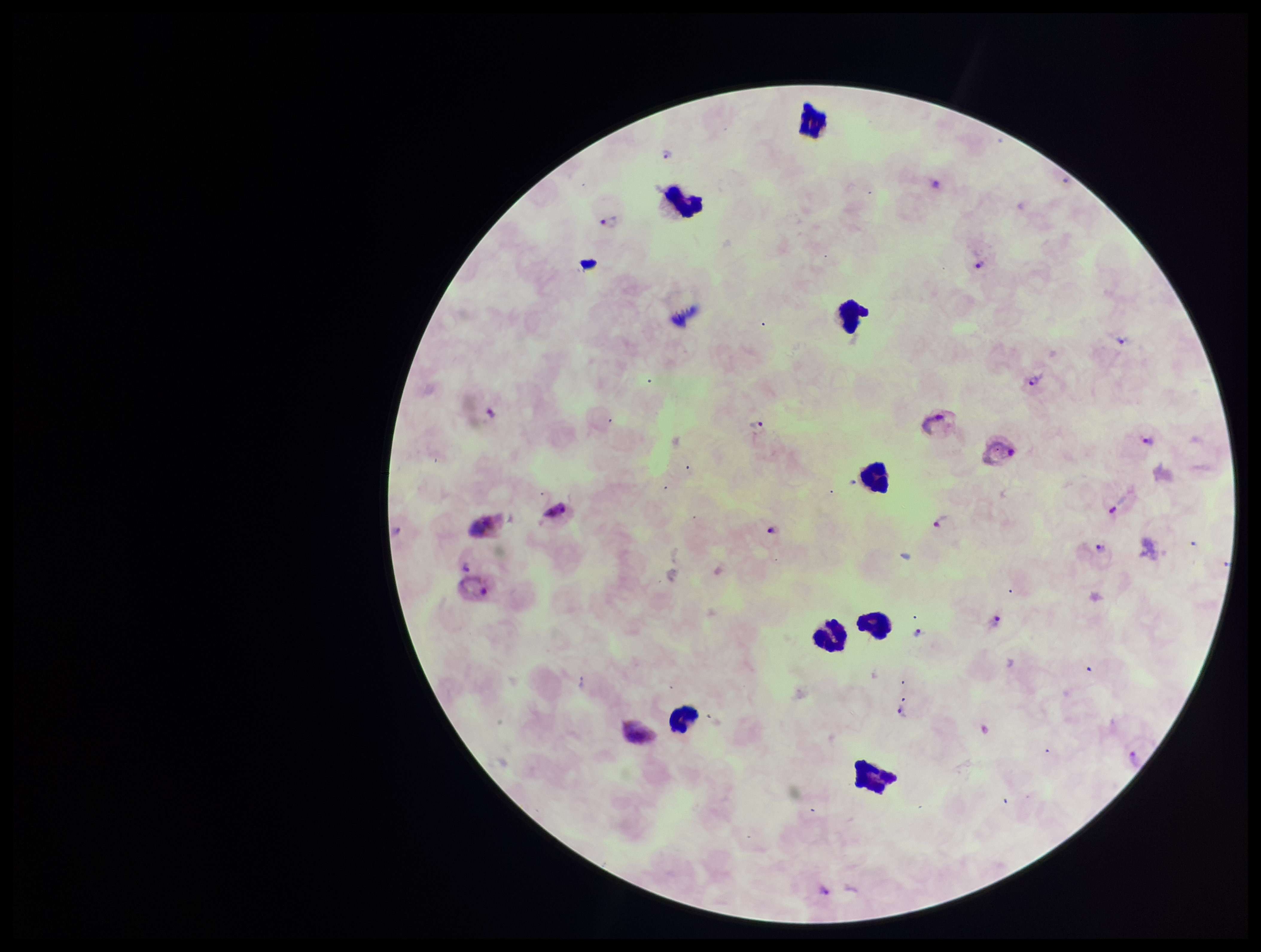

Leukocyte count: 8. Preparation: thick. One field from this slide. Stained with Giemsa. Species reported for this patient: Plasmodium vivax. Image is 1261×952 pixels. Parasite count: 14. Patient malaria status: positive. Plasmodium parasites: identified. Smartphone photograph taken through the eyepiece of a microscope.